Assess this cell for malaria.
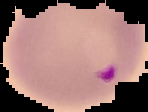

Parasitized.

Summary:
  - Preparation: thin blood film
  - Image size: 148×112 pixels
  - Image type: segmented cell region on a black background